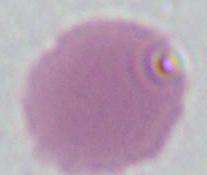
Summary:
  - Magnification: 1000x
  - Modality: photomicrograph
  - Identification: red blood cell